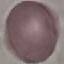
result: no malaria parasites detected
image_type: automatically extracted cell patch, resized to 64 × 64 pixels
preparation: thin smear
stain: Giemsa
capture: smartphone through the microscope eyepiece